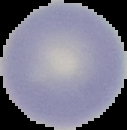

preparation = thin blood film
image size = 127×130 pixels
result = negative for malaria parasites
image type = segmented cell region on a black background